Locate every uninfected red blood cell.
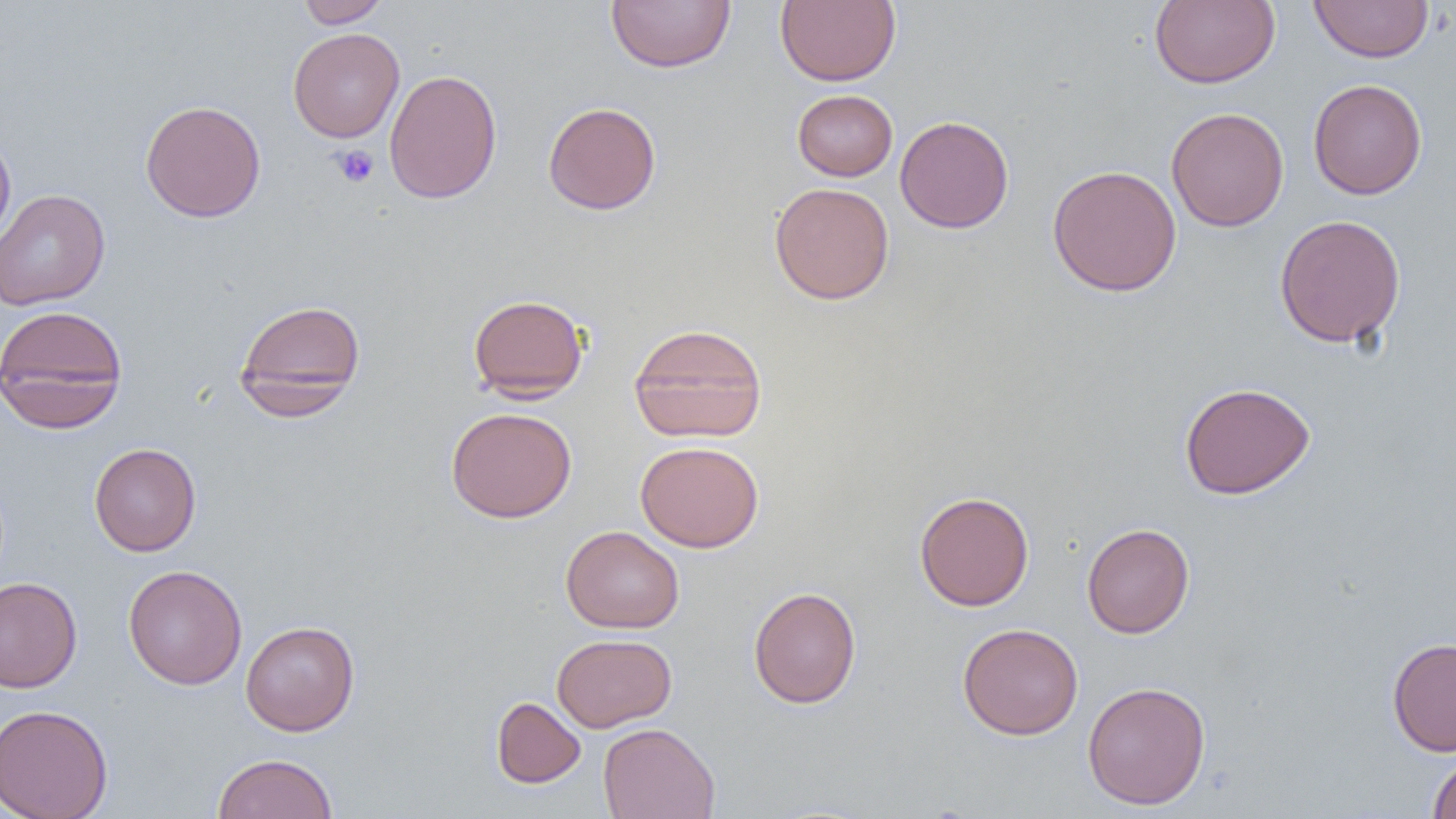
Approximate bounding boxes as (x1, y1, x2, y2) in pixels.
Uninfected red blood cells: (296, 0, 390, 28), (606, 0, 735, 73), (775, 0, 901, 87), (1149, 0, 1280, 88), (1308, 0, 1435, 63), (287, 27, 404, 143), (384, 69, 503, 204), (1308, 78, 1427, 199), (792, 89, 897, 181), (140, 99, 266, 223), (543, 101, 661, 215), (1166, 106, 1289, 232), (894, 115, 1014, 233), (0, 131, 16, 249), (1047, 164, 1182, 297), (769, 183, 895, 305), (0, 189, 110, 311), (1274, 214, 1406, 348), (468, 293, 589, 402), (234, 298, 366, 418), (0, 304, 128, 433), (628, 323, 768, 444), (1179, 381, 1315, 500), (446, 406, 576, 523), (635, 440, 764, 552), (88, 442, 201, 556), (914, 491, 1034, 611), (1081, 522, 1195, 639), (560, 525, 684, 633), (123, 564, 248, 690), (0, 577, 82, 692), (748, 586, 861, 708), (240, 620, 360, 736), (957, 623, 1084, 740), (552, 633, 677, 732), (1387, 636, 1456, 756), (1082, 680, 1211, 810), (491, 697, 586, 788), (0, 703, 113, 819), (597, 722, 721, 819), (212, 753, 338, 818), (1428, 754, 1456, 818).

Platelet locations: (330, 144, 380, 187). Slide-level diagnosis: negative for blood parasites. Single field of view. Image is 1456×819 pixels. 1000x magnification. Thin blood smear. Optical microscopy.